Give the location of every white blood cell.
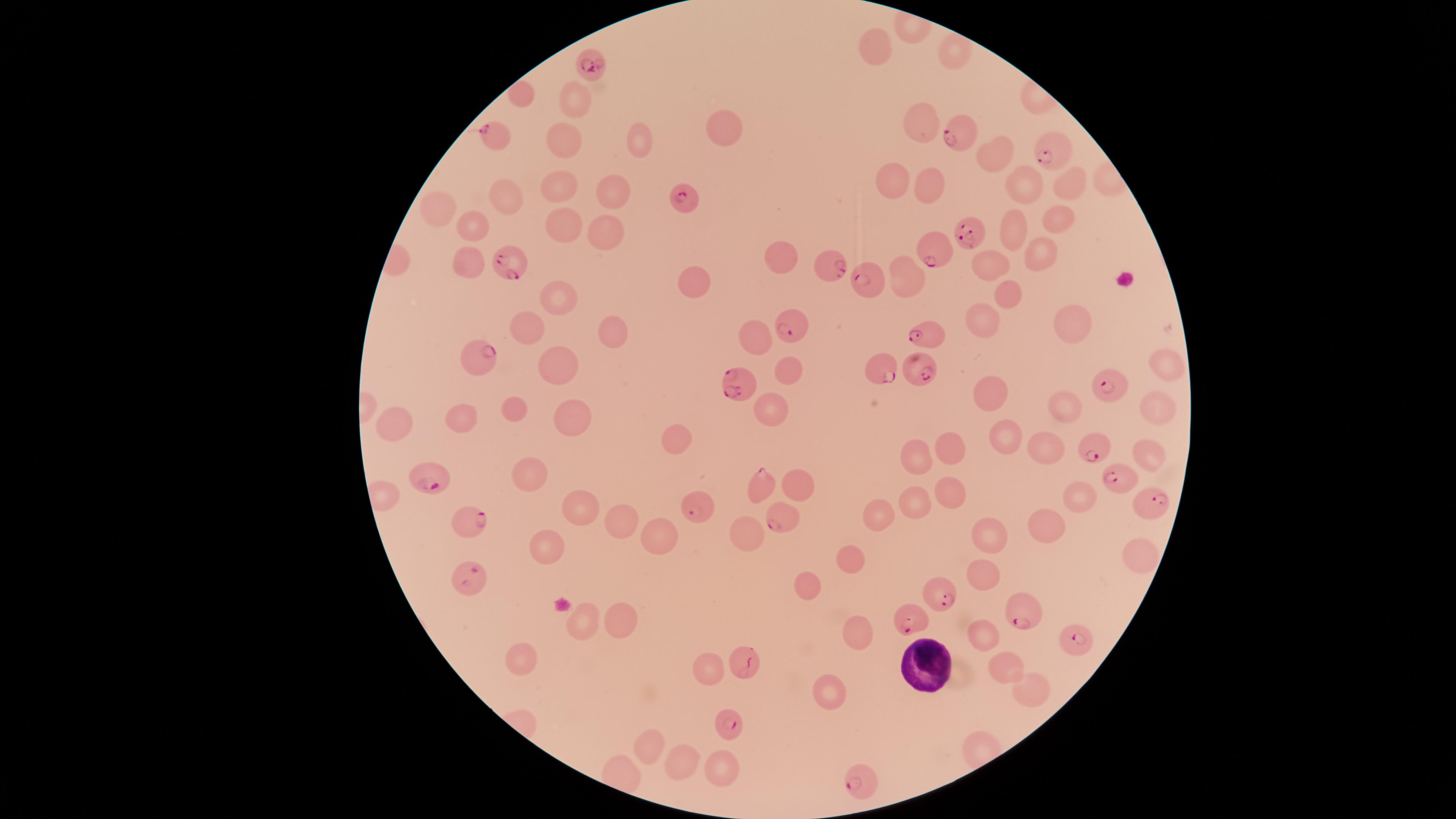

Approximate marker points as {x, y} in pixels.
White blood cells: {919, 663}.

Approximate marker points as {x, y} in pixels. Parasitized red blood cells: {588, 64}, {494, 133}, {959, 134}, {1049, 150}, {690, 199}, {971, 234}, {943, 248}, {509, 261}, {829, 263}, {867, 279}, {790, 327}, {926, 335}, {474, 361}, {918, 368}, {881, 369}, {1103, 379}, {737, 381}, {1090, 446}, {436, 475}, {1119, 477}, {761, 486}, {1148, 500}, {700, 509}, {471, 518}, {780, 519}, {471, 578}, {937, 593}, {1024, 612}, {909, 616}, {1076, 634}, {745, 666}, {731, 724}, {861, 780}. Uninfected red blood cells: {876, 45}, {953, 50}, {522, 91}, {573, 98}, {919, 123}, {716, 129}, {568, 139}, {644, 139}, {995, 153}, {887, 177}, {1022, 181}, {1065, 183}, {560, 184}, {932, 184}, {610, 188}, {504, 196}, {439, 206}, {1056, 222}, {473, 224}, {560, 226}, {595, 227}, {1013, 227}, {1037, 252}, {784, 258}, {468, 265}, {988, 265}, {908, 275}, {695, 284}, {1008, 294}, {558, 296}, {1068, 318}, {981, 321}, {525, 327}, {611, 330}, {755, 335}, {568, 361}, {791, 364}, {1159, 366}, {992, 390}, {1061, 400}, {773, 402}, {1156, 402}, {513, 408}, {394, 418}, {463, 418}, {570, 418}, {1011, 431}, {675, 435}, {1041, 446}, {952, 448}, {918, 457}, {530, 478}, {802, 481}, {946, 489}, {1080, 495}, {914, 500}, {583, 505}, {626, 516}, {880, 517}, {1054, 523}, {989, 531}, {661, 533}, {746, 533}, {550, 551}, {851, 557}, {1136, 559}, {981, 570}, {814, 585}, {622, 613}, {587, 618}, {854, 631}, {981, 634}, {527, 650}, {1003, 660}, {709, 670}, {828, 691}, {1029, 691}, {649, 750}, {717, 763}, {678, 764}. Image is 1456×819 pixels. Presence: malaria parasites seen. Single field of view. Species: Plasmodium falciparum. Giemsa-stained preparation. The visible region is circular. Thin blood film. Smartphone photograph through the microscope eyepiece.